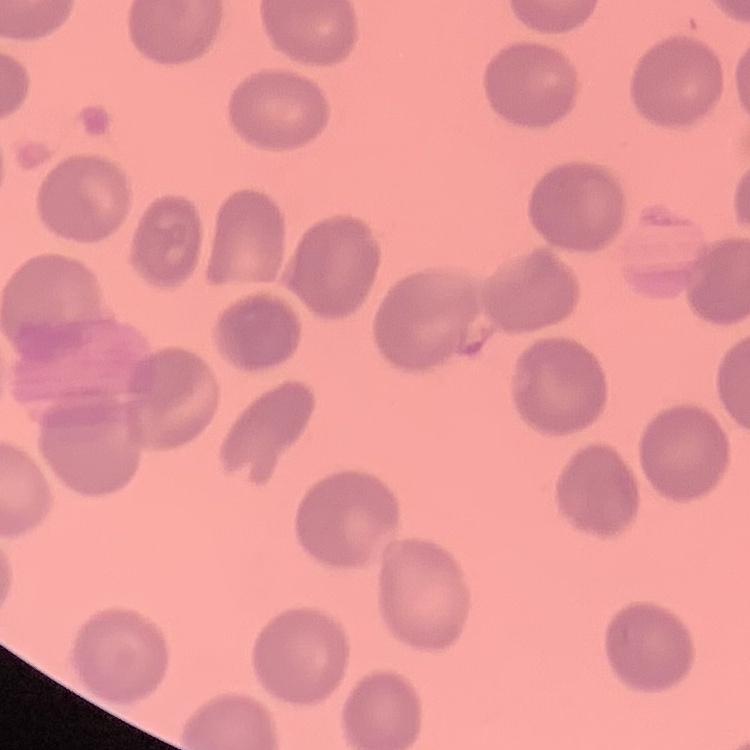
The red blood cells show no rouleaux formation. Field's or Giemsa stain. Thin blood smear. Square crop of a larger photomicrograph.